Classify this cell by malaria status.
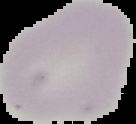
It is uninfected.

preparation = thin blood film
image type = segmented cell region with the area outside set to black
image size = 136×124 pixels